Name the blood parasite species.
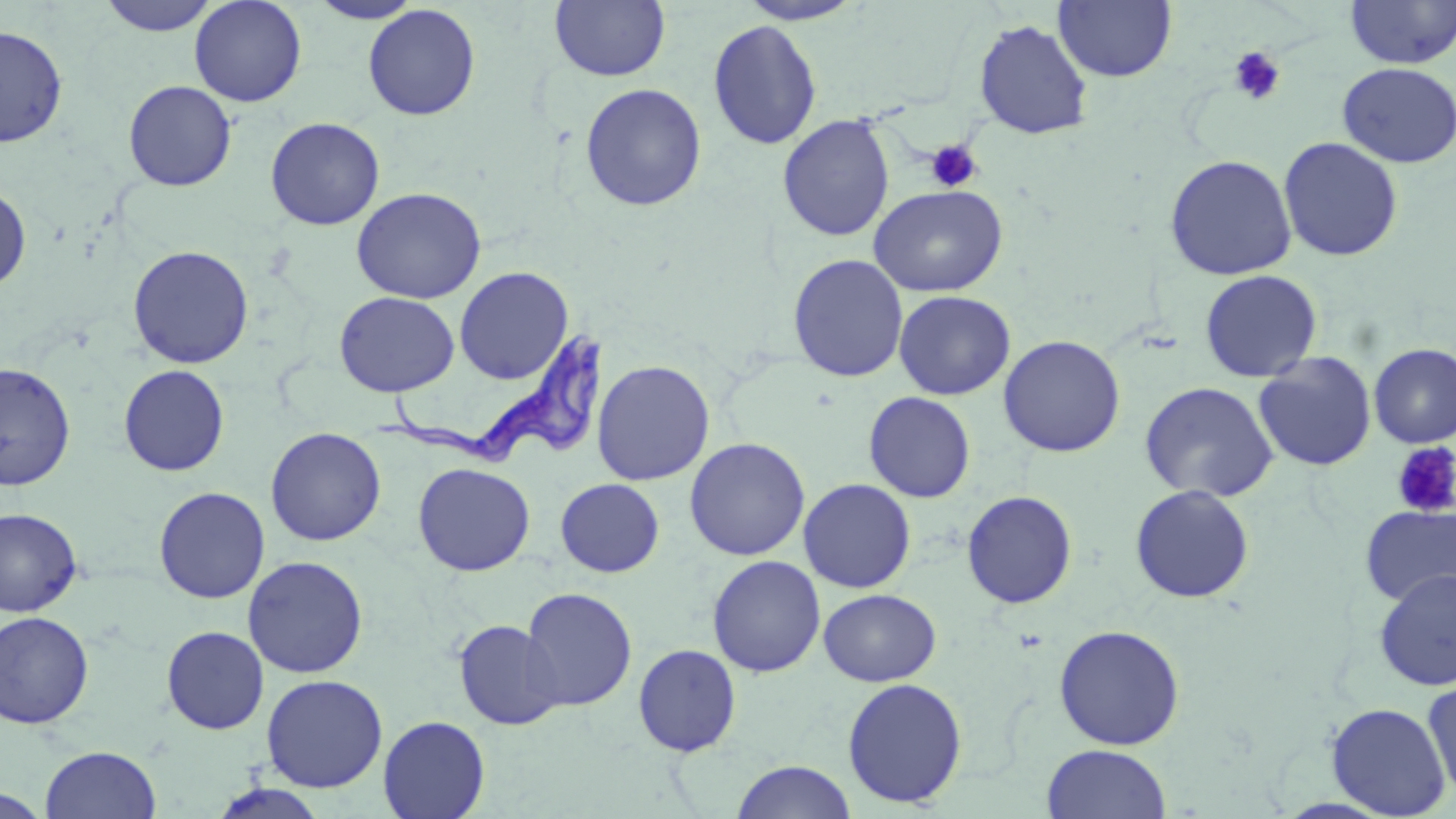
Trypanosoma brucei.

{
  "uninfected_red_blood_cell_locations": "approximate bounding boxes as named x1/y1/x2/y2 corners in pixels: (x1=96, y1=0, x2=222, y2=36), (x1=189, y1=0, x2=307, y2=107), (x1=307, y1=0, x2=425, y2=24), (x1=736, y1=0, x2=868, y2=25), (x1=1344, y1=0, x2=1456, y2=69), (x1=549, y1=1, x2=670, y2=82), (x1=1054, y1=1, x2=1177, y2=83), (x1=362, y1=4, x2=481, y2=121), (x1=707, y1=19, x2=823, y2=150), (x1=973, y1=19, x2=1093, y2=140), (x1=0, y1=25, x2=68, y2=148), (x1=1337, y1=62, x2=1456, y2=168), (x1=123, y1=80, x2=237, y2=192), (x1=579, y1=83, x2=706, y2=212), (x1=777, y1=114, x2=895, y2=242), (x1=265, y1=116, x2=385, y2=230), (x1=1278, y1=136, x2=1404, y2=262), (x1=1164, y1=154, x2=1297, y2=281), (x1=0, y1=185, x2=31, y2=292), (x1=869, y1=185, x2=1008, y2=297), (x1=350, y1=187, x2=486, y2=304), (x1=128, y1=245, x2=254, y2=369), (x1=788, y1=254, x2=908, y2=383), (x1=454, y1=266, x2=574, y2=384), (x1=1199, y1=270, x2=1322, y2=382), (x1=893, y1=290, x2=1015, y2=400), (x1=333, y1=291, x2=460, y2=397), (x1=998, y1=335, x2=1126, y2=458), (x1=1369, y1=342, x2=1456, y2=448), (x1=1253, y1=352, x2=1377, y2=471), (x1=592, y1=359, x2=715, y2=486), (x1=0, y1=362, x2=76, y2=490), (x1=119, y1=364, x2=230, y2=476), (x1=1139, y1=381, x2=1279, y2=503), (x1=863, y1=391, x2=976, y2=503), (x1=265, y1=427, x2=386, y2=546), (x1=684, y1=437, x2=810, y2=561), (x1=413, y1=462, x2=535, y2=576), (x1=555, y1=478, x2=664, y2=577), (x1=798, y1=478, x2=916, y2=593), (x1=1129, y1=484, x2=1254, y2=603), (x1=154, y1=486, x2=270, y2=603), (x1=961, y1=490, x2=1078, y2=609), (x1=1359, y1=503, x2=1456, y2=607), (x1=0, y1=508, x2=82, y2=617), (x1=242, y1=555, x2=369, y2=679), (x1=707, y1=555, x2=826, y2=677), (x1=1374, y1=568, x2=1456, y2=692), (x1=520, y1=587, x2=637, y2=711), (x1=818, y1=588, x2=941, y2=686), (x1=0, y1=610, x2=94, y2=729), (x1=453, y1=620, x2=565, y2=730), (x1=1053, y1=624, x2=1185, y2=750), (x1=161, y1=626, x2=269, y2=734), (x1=632, y1=643, x2=741, y2=757), (x1=261, y1=674, x2=388, y2=792), (x1=1421, y1=676, x2=1456, y2=803), (x1=842, y1=677, x2=968, y2=808), (x1=1325, y1=702, x2=1452, y2=817), (x1=378, y1=715, x2=490, y2=819), (x1=1041, y1=744, x2=1172, y2=819), (x1=40, y1=745, x2=161, y2=819), (x1=731, y1=760, x2=857, y2=819), (x1=207, y1=783, x2=330, y2=819), (x1=0, y1=785, x2=52, y2=817)",
  "preparation": "thin blood smear",
  "trypanosoma_brucei_locations": "approximate bounding boxes as named x1/y1/x2/y2 corners in pixels: (x1=375, y1=325, x2=614, y2=470)",
  "modality": "optical microscopy",
  "magnification": "1000x",
  "field_of_view": "one of a larger specimen",
  "image_size": "1456×819 pixels",
  "stain": "May-Grünwald-Giemsa",
  "platelet_locations": "approximate bounding boxes as named x1/y1/x2/y2 corners in pixels: (x1=1227, y1=46, x2=1286, y2=106), (x1=924, y1=139, x2=983, y2=193), (x1=1390, y1=442, x2=1456, y2=519)"
}